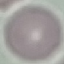
Summary:
  - Malaria status: uninfected
  - Stain: Giemsa
  - Capture: smartphone camera at the microscope eyepiece
  - Preparation: thin blood film
  - Image type: automatically extracted cell patch, resized to 64 × 64 pixels